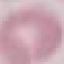
Result: negative for malaria parasites. Photographed with a smartphone camera at the microscope eyepiece. Giemsa stain. Thin blood smear. Automatically extracted cell patch, resized to 64 × 64 pixels.